Give the position of every leukocyte visible.
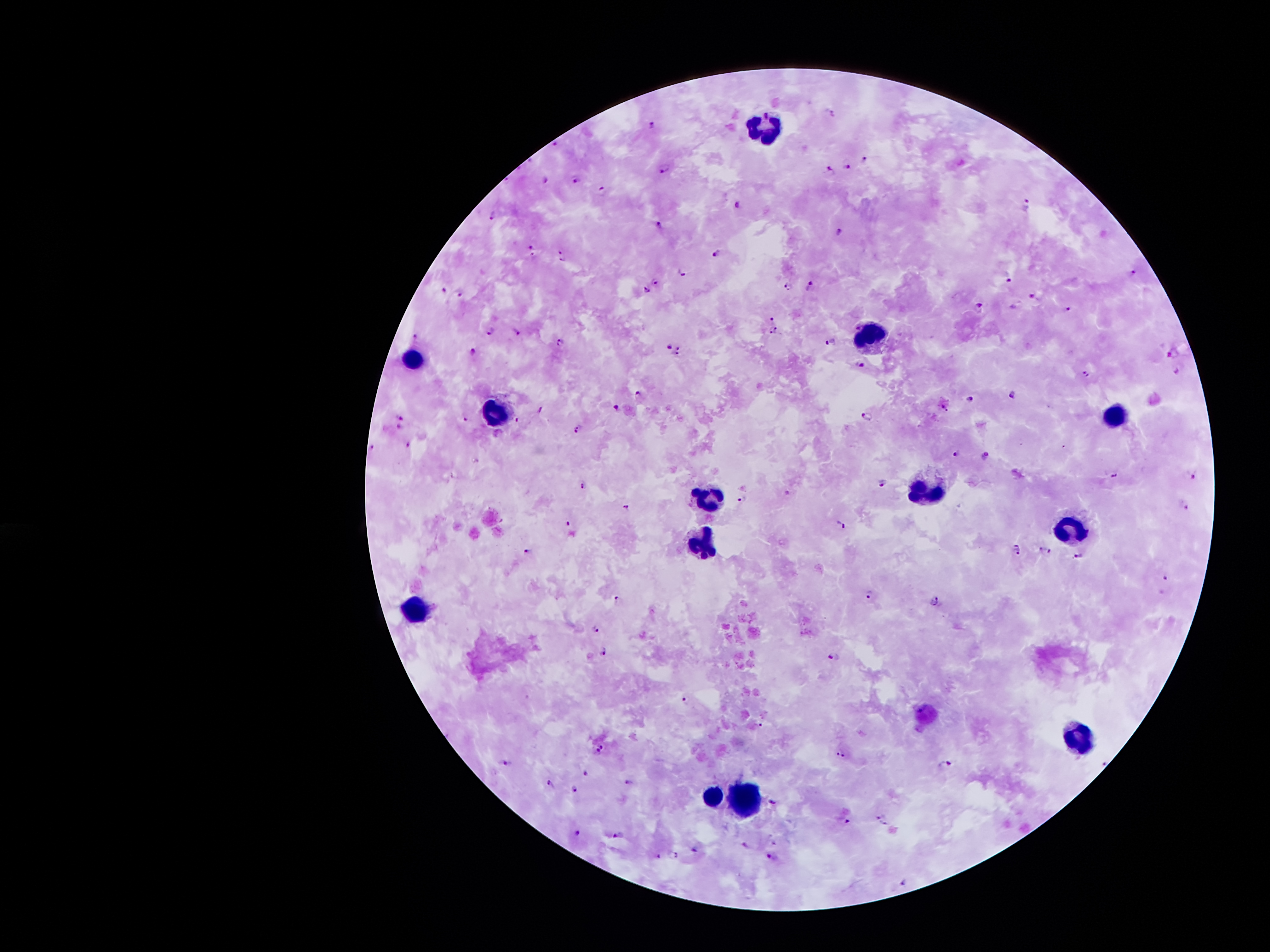

Approximate centers as {x, y} in pixels.
Leukocytes: {759, 129}, {875, 336}, {415, 357}, {501, 412}, {1118, 413}, {934, 486}, {709, 492}, {1072, 525}, {699, 544}, {412, 612}, {1077, 730}, {714, 791}, {751, 794}.

Malaria parasite locations: {652, 124}, {554, 143}, {865, 158}, {847, 166}, {666, 168}, {832, 171}, {576, 178}, {547, 181}, {602, 191}, {1027, 202}, {737, 204}, {494, 214}, {658, 225}, {841, 231}, {532, 248}, {717, 254}, {562, 255}, {1132, 271}, {683, 272}, {1009, 278}, {655, 281}, {810, 285}, {789, 287}, {445, 289}, {647, 290}, {461, 295}, {1035, 295}, {980, 309}, {1070, 309}, {772, 319}, {491, 331}, {773, 331}, {517, 332}, {414, 336}, {831, 341}, {561, 343}, {670, 347}, {679, 348}, {473, 352}, {675, 354}, {1174, 355}, {860, 365}, {1176, 370}, {1086, 371}, {1013, 394}, {638, 395}, {969, 398}, {943, 406}, {617, 407}, {540, 408}, {867, 416}, {401, 418}, {518, 419}, {465, 420}, {398, 427}, {578, 430}, {408, 444}, {373, 447}, {958, 454}, {984, 456}, {1115, 476}, {1195, 476}, {882, 481}, {584, 482}, {743, 499}, {625, 506}, {1185, 506}, {567, 521}, {841, 524}, {1042, 547}, {1020, 551}, {1050, 552}, {527, 553}, {1079, 555}, {1167, 577}, {869, 593}, {619, 598}, {935, 600}, {596, 628}, {605, 652}, {834, 655}, {686, 699}, {761, 725}, {603, 745}, {598, 752}, {840, 752}, {505, 762}, {946, 762}, {585, 772}, {629, 782}, {550, 783}, {574, 788}, {773, 801}, {880, 816}, {844, 821}, {886, 824}, {578, 833}, {618, 835}, {774, 843}, {745, 845}, {696, 849}, {675, 853}, {658, 854}, {772, 855}, {904, 883}. 100x magnification. Smartphone photograph taken through the microscope eyepiece. Patient malaria status: infected with Plasmodium falciparum. Thick blood smear. One field from this slide. Giemsa-stained preparation. Image is 1270×952 pixels.